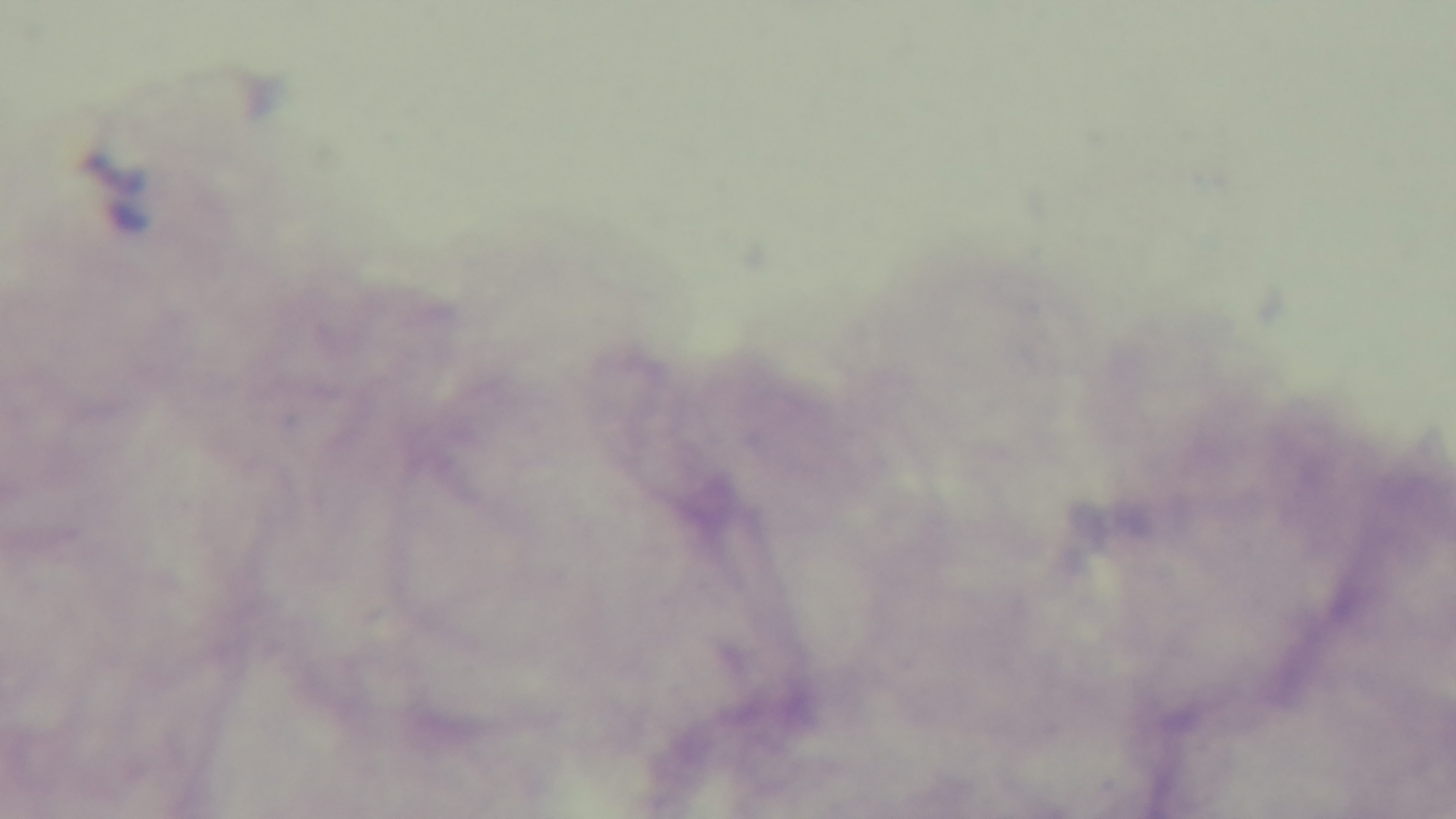
Summary:
  - Malaria status: negative
  - Stain: Giemsa
  - Objective: 100x oil immersion
  - Field of view: single
  - Preparation: thick blood film
  - Capture: mounted 4K digital camera
  - Modality: light microscopy